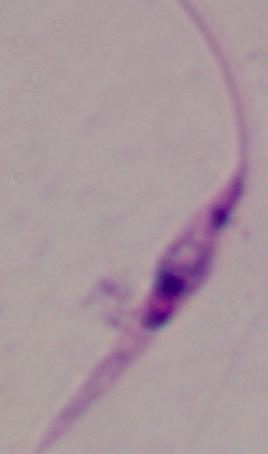

Photomicrograph. Captured at 1000x magnification. A Leishmania parasite is seen.